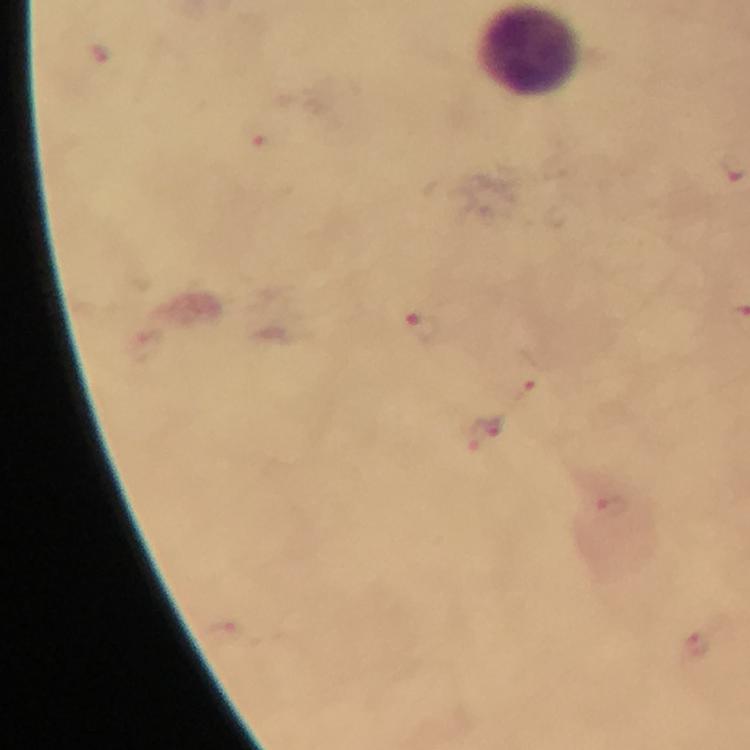
Approximate centers as (x, y) in pixels. Malaria parasite locations: (260, 138), (420, 325), (523, 386), (483, 429), (610, 506), (696, 645). Image is 750×750 pixels. A crop from one field of view. Photographed with a smartphone mounted on the microscope. From a diagnostic examination for malaria. Thick blood film. Giemsa stain. At 100x magnification. Immersion oil applied.